Report the malaria status of this cell.
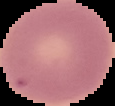
It is uninfected.

preparation = thin blood smear
image type = segmented cell region with the area outside set to black
image size = 115×106 pixels